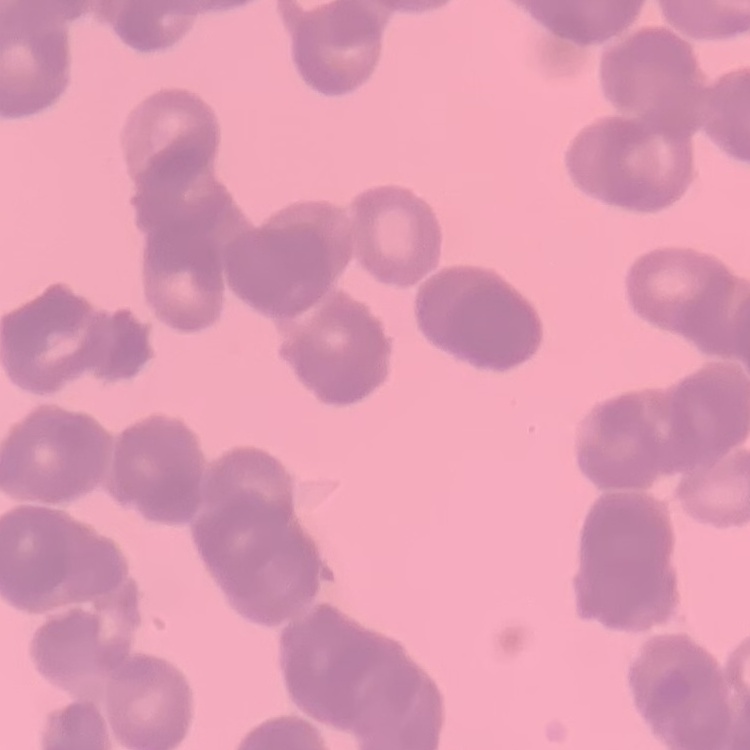

The erythrocytes exhibit rouleaux formation. Thin blood smear. Field's or Giemsa stain. Square crop of a larger photomicrograph.